Locate every Plasmodium parasite.
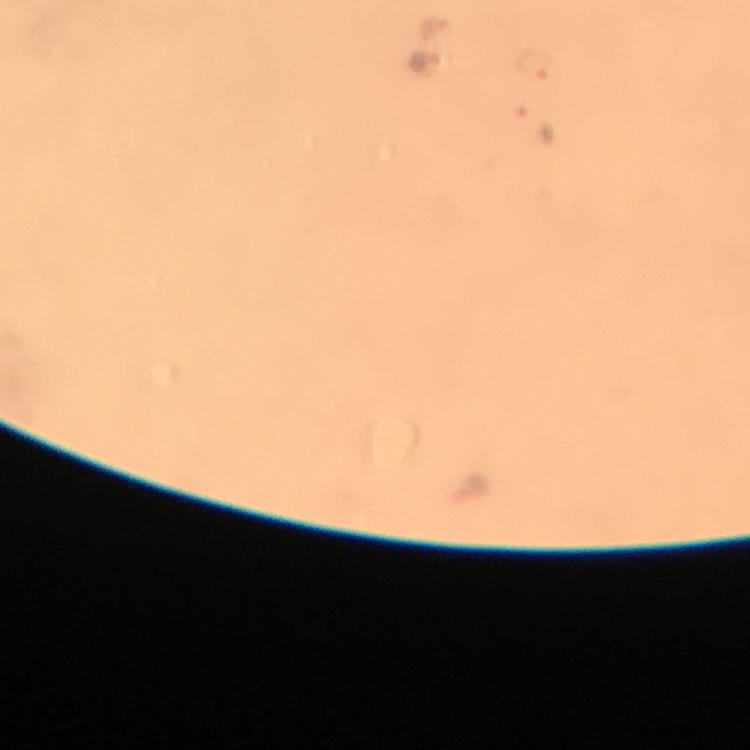
Approximate centers as [x, y] in pixels.
Plasmodium parasites: [433, 29], [422, 60], [530, 68], [531, 122].

Summary:
  - Image size: 750×750 pixels
  - Capture: smartphone photograph through a microscope
  - Context: from a malaria diagnostic workup
  - Cropped from: a single field of view
  - Preparation: thick blood smear
  - Magnification: 100x
  - Stain: Giemsa
  - Immersion oil: applied